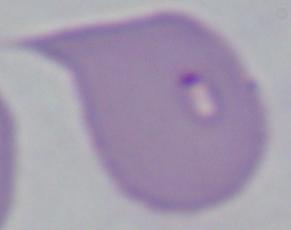

magnification = 1000x
identification = Babesia
modality = photomicrograph